State which parasite is depicted.
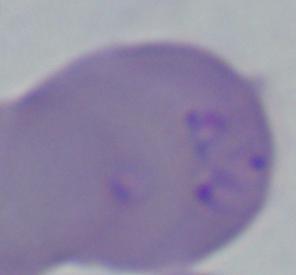
Babesia.

Micrograph. 1000x magnification.